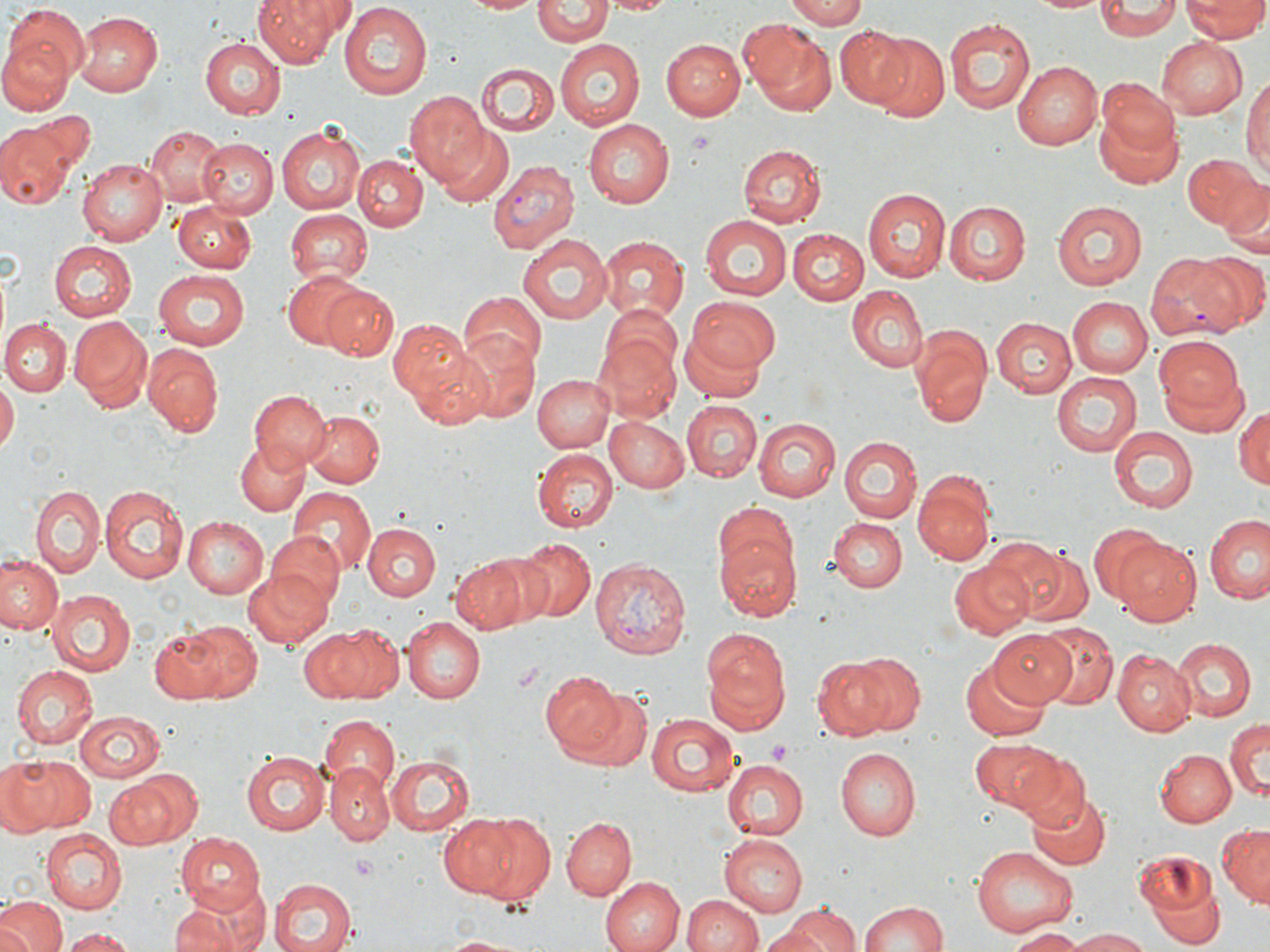
slide-level diagnosis = Plasmodium vivax
stain = May-Grünwald-Giemsa
magnification = 1000x
image size = 1270×952 pixels
preparation = thin blood film
modality = light microscopy
field of view = single
Plasmodium vivax-infected red blood cell locations = approximate bounding boxes as [x1, y1, x2, y2] in pixels: [487, 159, 578, 255], [1149, 251, 1246, 342], [589, 555, 692, 661]
uninfected red blood cell locations = approximate bounding boxes as [x1, y1, x2, y2] in pixels: [252, 0, 347, 68], [462, 0, 543, 15], [602, 0, 677, 15], [784, 0, 868, 27], [1029, 0, 1110, 15], [534, 1, 609, 46], [1098, 1, 1180, 39], [1182, 1, 1270, 41], [5, 5, 89, 85], [339, 6, 430, 97], [74, 12, 162, 98], [943, 17, 1037, 113], [744, 19, 837, 112], [835, 25, 918, 111], [0, 33, 74, 114], [873, 36, 949, 123], [200, 38, 287, 118], [661, 38, 745, 119], [1157, 38, 1247, 118], [552, 39, 647, 131], [1010, 60, 1101, 150], [475, 63, 559, 139], [1242, 70, 1270, 179], [1095, 80, 1178, 161], [406, 92, 491, 184], [1094, 112, 1184, 191], [0, 118, 81, 208], [583, 118, 675, 208], [279, 123, 364, 214], [434, 124, 513, 206], [144, 125, 227, 207], [198, 139, 276, 220], [738, 144, 827, 227], [1184, 152, 1262, 232], [352, 154, 427, 231], [76, 158, 167, 245], [1217, 177, 1269, 253], [865, 188, 950, 281], [1055, 200, 1147, 289], [944, 202, 1030, 285], [173, 204, 257, 273], [283, 210, 370, 287], [700, 215, 792, 300], [789, 228, 868, 305], [514, 233, 617, 325], [597, 236, 686, 324], [48, 240, 137, 321], [1189, 252, 1269, 334], [153, 269, 248, 349], [283, 271, 369, 351], [322, 285, 398, 361], [848, 286, 927, 371], [458, 294, 546, 372], [685, 295, 782, 379], [316, 297, 456, 369], [1069, 298, 1152, 376], [594, 307, 684, 417], [993, 314, 1078, 396], [68, 316, 153, 411], [2, 319, 72, 396], [390, 319, 471, 399], [679, 329, 769, 403], [910, 329, 990, 427], [454, 330, 540, 421], [1153, 334, 1246, 427], [142, 344, 223, 438], [410, 345, 497, 430], [1052, 370, 1143, 458], [535, 375, 614, 453], [0, 382, 17, 457], [247, 389, 328, 471], [680, 399, 763, 480], [1234, 404, 1270, 491], [303, 409, 384, 488], [604, 416, 690, 493], [752, 417, 841, 501], [1108, 427, 1196, 513], [838, 437, 920, 524], [235, 440, 310, 516], [534, 451, 617, 533], [915, 474, 995, 565], [100, 484, 187, 583], [30, 486, 104, 577], [287, 488, 374, 580], [1204, 514, 1270, 603], [184, 517, 268, 599], [828, 517, 906, 592], [364, 523, 441, 602], [714, 524, 800, 623], [1091, 525, 1174, 605], [266, 532, 348, 611], [1113, 536, 1202, 626], [516, 537, 595, 621], [996, 542, 1090, 629], [474, 549, 567, 628], [0, 554, 61, 635], [451, 554, 531, 632], [950, 562, 1030, 640], [243, 566, 333, 649], [45, 589, 135, 678], [403, 615, 486, 703], [170, 619, 263, 704], [1034, 621, 1117, 710], [297, 624, 399, 705], [701, 627, 790, 734], [986, 629, 1078, 703], [1171, 637, 1257, 721], [1111, 649, 1195, 735], [844, 652, 925, 735], [811, 654, 898, 740], [960, 661, 1050, 742], [10, 664, 98, 750], [541, 670, 624, 757], [562, 682, 653, 770], [74, 711, 165, 782], [646, 712, 739, 796], [317, 717, 400, 795], [1225, 720, 1268, 802], [969, 737, 1060, 814], [835, 747, 922, 841], [241, 749, 328, 836], [1156, 749, 1236, 828], [1011, 752, 1092, 830], [386, 754, 474, 835], [1, 758, 93, 834], [722, 758, 807, 841], [327, 762, 393, 844], [104, 774, 188, 849], [1028, 790, 1110, 871], [443, 812, 556, 903], [561, 818, 635, 899], [1218, 825, 1270, 906], [43, 829, 127, 913], [174, 832, 264, 910], [720, 835, 808, 916], [971, 844, 1079, 938], [1130, 850, 1225, 948], [600, 876, 682, 952], [270, 877, 356, 952], [682, 893, 762, 952], [0, 896, 66, 952], [168, 897, 263, 952], [858, 899, 951, 952], [781, 903, 862, 951], [1006, 928, 1085, 950], [62, 929, 136, 952], [756, 929, 832, 952], [1066, 929, 1153, 952], [438, 933, 538, 952]
platelet locations = approximate bounding boxes as [x1, y1, x2, y2] in pixels: [767, 740, 790, 763], [353, 853, 378, 883]